Name the blood parasite species.
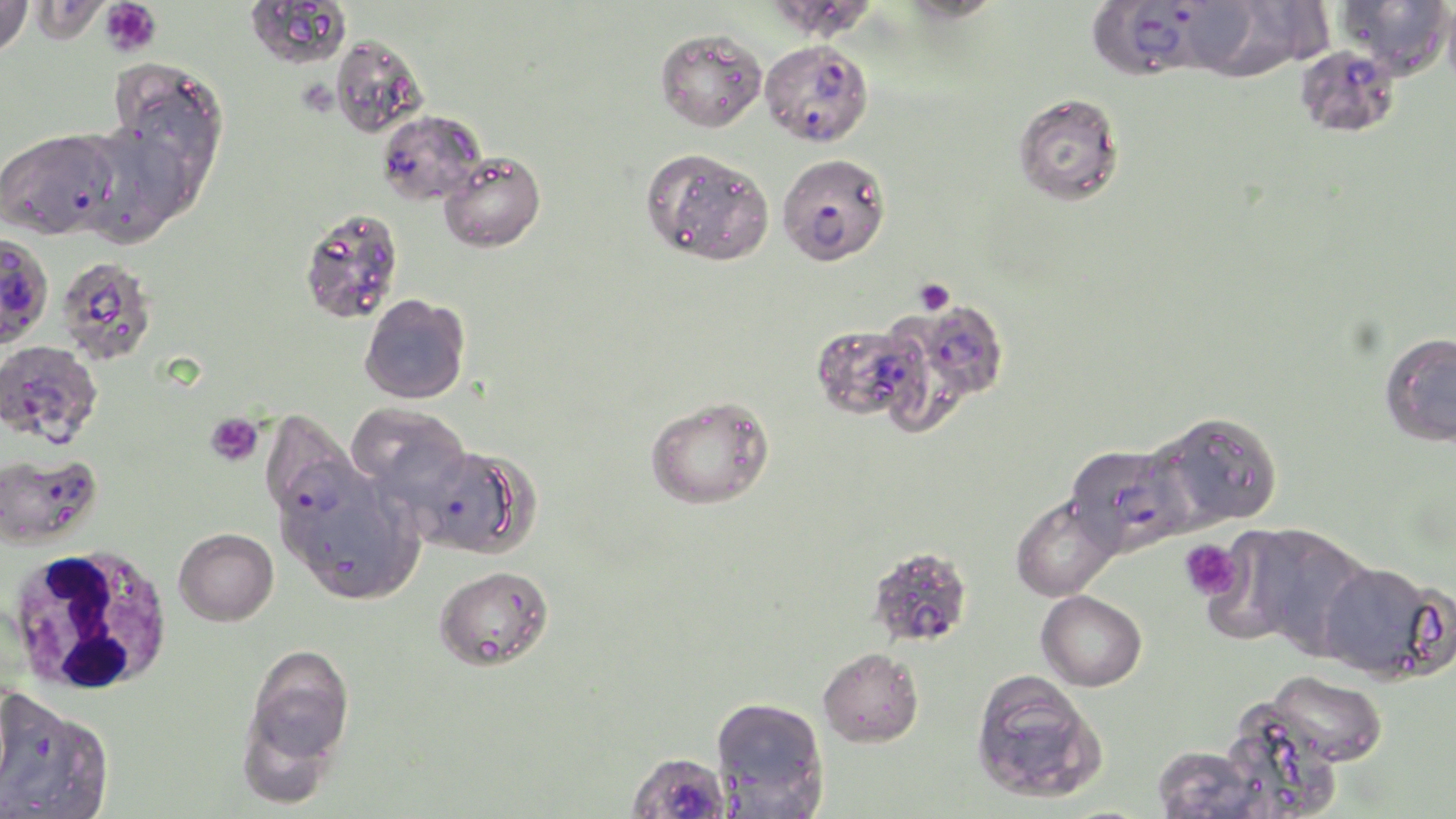
Plasmodium falciparum.

uninfected red blood cell locations = approximate bounding boxes as (x1, y1, x2, y2) in pixels: (0, 0, 35, 60), (764, 0, 881, 41), (899, 0, 1004, 24), (1337, 0, 1454, 79), (1185, 1, 1323, 80), (655, 28, 767, 132), (330, 35, 427, 139), (102, 59, 225, 192), (1013, 93, 1125, 206), (74, 121, 197, 248), (640, 146, 774, 266), (439, 151, 546, 253), (298, 206, 404, 325), (360, 293, 471, 404), (903, 300, 1009, 404), (812, 323, 927, 422), (1379, 332, 1456, 447), (644, 395, 775, 509), (346, 403, 471, 507), (1157, 411, 1284, 529), (277, 465, 423, 605), (1010, 495, 1120, 602), (1226, 523, 1373, 657), (173, 527, 278, 626), (1317, 561, 1446, 682), (434, 566, 554, 671), (1036, 590, 1147, 691), (244, 645, 354, 767), (818, 647, 923, 747), (1265, 669, 1389, 767), (970, 670, 1107, 804), (1, 690, 114, 818), (711, 696, 828, 812), (235, 706, 340, 811), (1222, 707, 1342, 819), (1151, 744, 1271, 818)
magnification = 1000x
platelet locations = approximate bounding boxes as (x1, y1, x2, y2) in pixels: (100, 0, 161, 57), (913, 277, 955, 316), (204, 412, 263, 467), (1178, 539, 1246, 602)
preparation = thin blood smear
stain = May-Grünwald-Giemsa
Plasmodium falciparum-infected red blood cell locations = approximate bounding boxes as (x1, y1, x2, y2) in pixels: (1088, 1, 1212, 80), (759, 39, 874, 147), (1294, 45, 1400, 139), (377, 110, 486, 207), (0, 129, 120, 240), (777, 153, 891, 266), (0, 232, 54, 348), (57, 256, 157, 366), (0, 339, 102, 446), (261, 412, 360, 522), (1065, 442, 1192, 556), (410, 447, 506, 554), (0, 449, 102, 549), (872, 551, 969, 650), (624, 751, 733, 819)
field of view = one of a larger specimen
white blood cell locations = approximate bounding boxes as (x1, y1, x2, y2) in pixels: (5, 544, 175, 696)
modality = optical microscopy
image size = 1456×819 pixels